Comment on the morphology of the red blood cells.
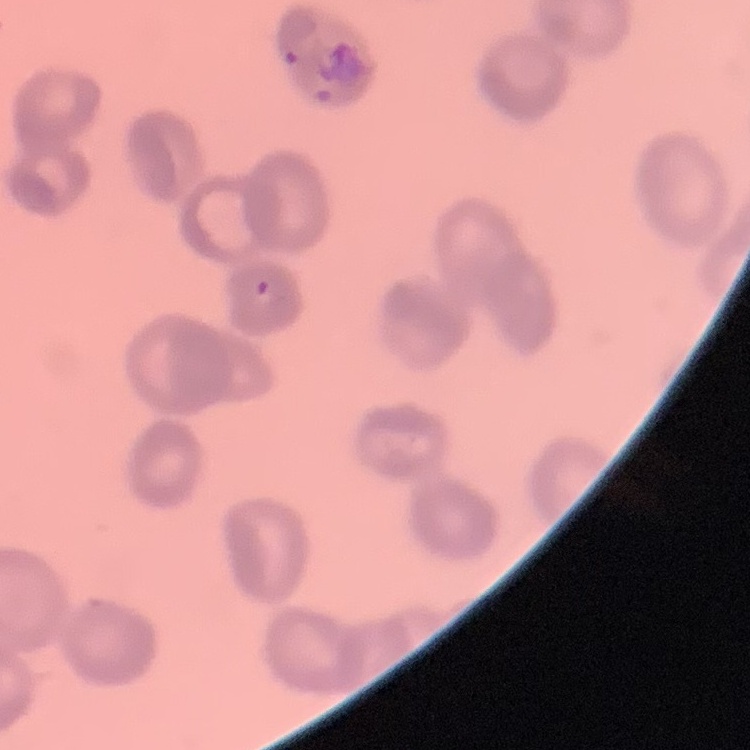

Rouleaux formation.

Thin peripheral smear. Stained with either Field's or Giemsa. One tile cut from a larger photomicrograph.